Report the malaria status of this cell.
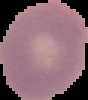
Uninfected.

image_size: 88×100 pixels
preparation: thin blood film
image_type: cell region segmented out of the field of view; surrounding area masked to black